Report the malaria status of this cell.
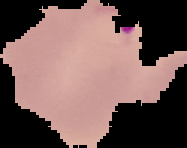
It is parasitized.

image type = cell region segmented out of the field of view; surrounding area masked to black
image size = 187×148 pixels
preparation = thin blood smear